Classify this cell by malaria status.
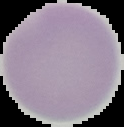

It is uninfected.

From a thin blood film. Image is 124×127 pixels. Segmented cell region on a black background.